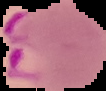
{
  "malaria_status": "parasitized",
  "preparation": "thin blood film",
  "image_type": "cell region segmented out of the field of view; surrounding area masked to black",
  "image_size": "106×91 pixels"
}